Look for Plasmodium parasites.
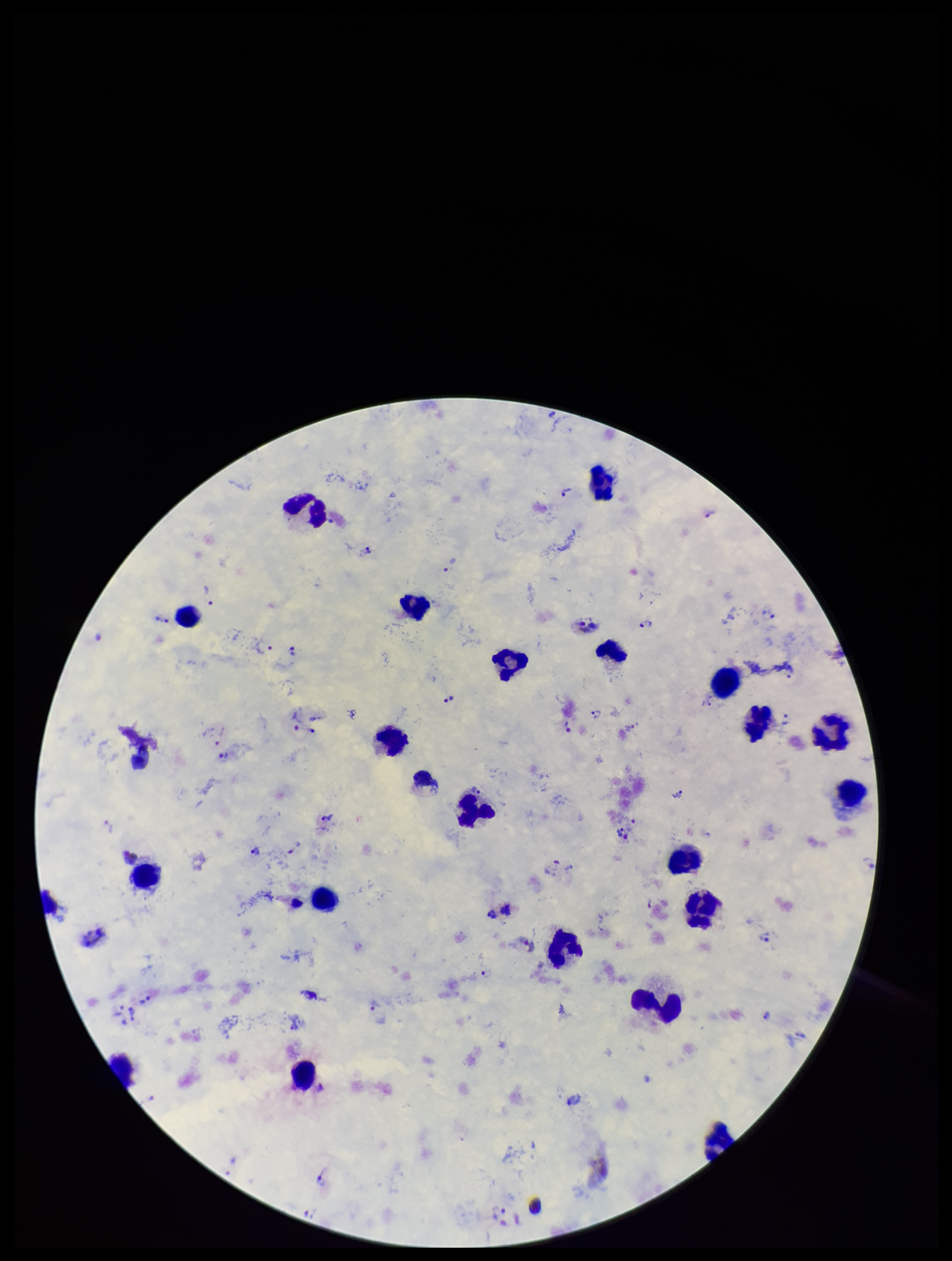
Identified.

Summary:
  - Preparation: thick smear
  - Species reported for this patient: Plasmodium vivax
  - Patient malaria status: infected
  - Capture: smartphone photograph through the microscope eyepiece
  - Image size: 952×1261 pixels
  - Stain: Giemsa
  - Parasite count: 35
  - Field of view: single
  - Leukocyte count: 23